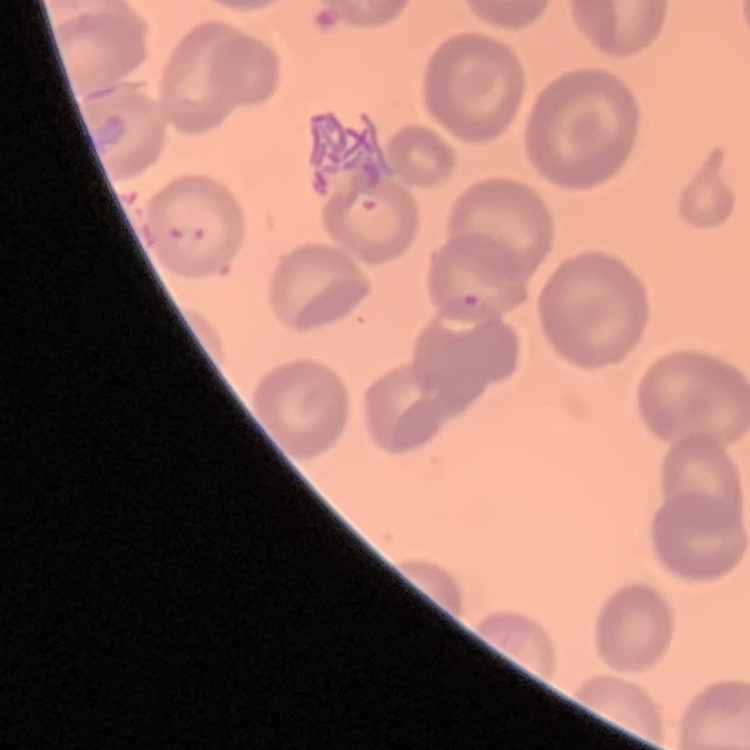
Summary:
  - Erythrocyte morphology: no rouleaux formation
  - Stain: Field's or Giemsa
  - Image type: square crop of a larger photomicrograph
  - Preparation: thin blood film